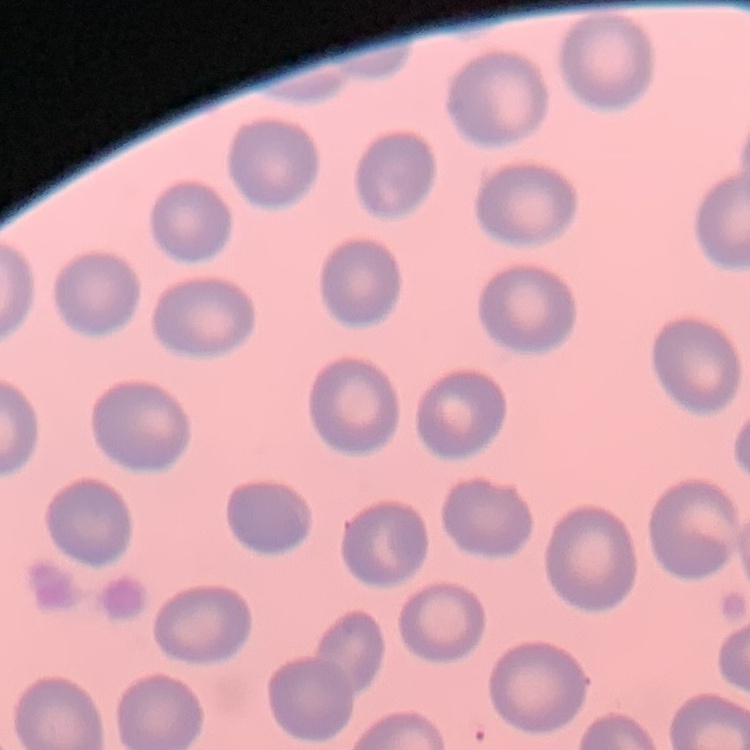

red blood cell morphology = no rouleaux formation
image type = one tile cut from a larger photomicrograph
stain = Field's or Giemsa
preparation = thin blood film